State which cell type is depicted.
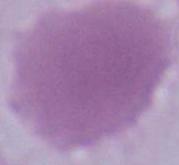
An erythrocyte.

magnification: 1000x
modality: photomicrograph